Report the malaria status of this cell.
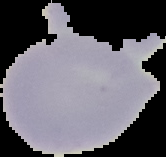

It is uninfected.

{
  "preparation": "thin blood film",
  "image_size": "166×157 pixels",
  "image_type": "cell region segmented out of the field of view; surrounding area masked to black"
}